Identify the parasite.
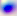
Toxoplasma gondii.

magnification = 400x
modality = photomicrograph